State which parasite is depicted.
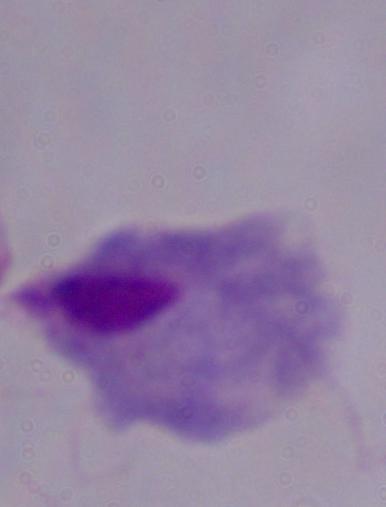
A trichomonad.

Summary:
  - Modality: micrograph
  - Magnification: 1000x